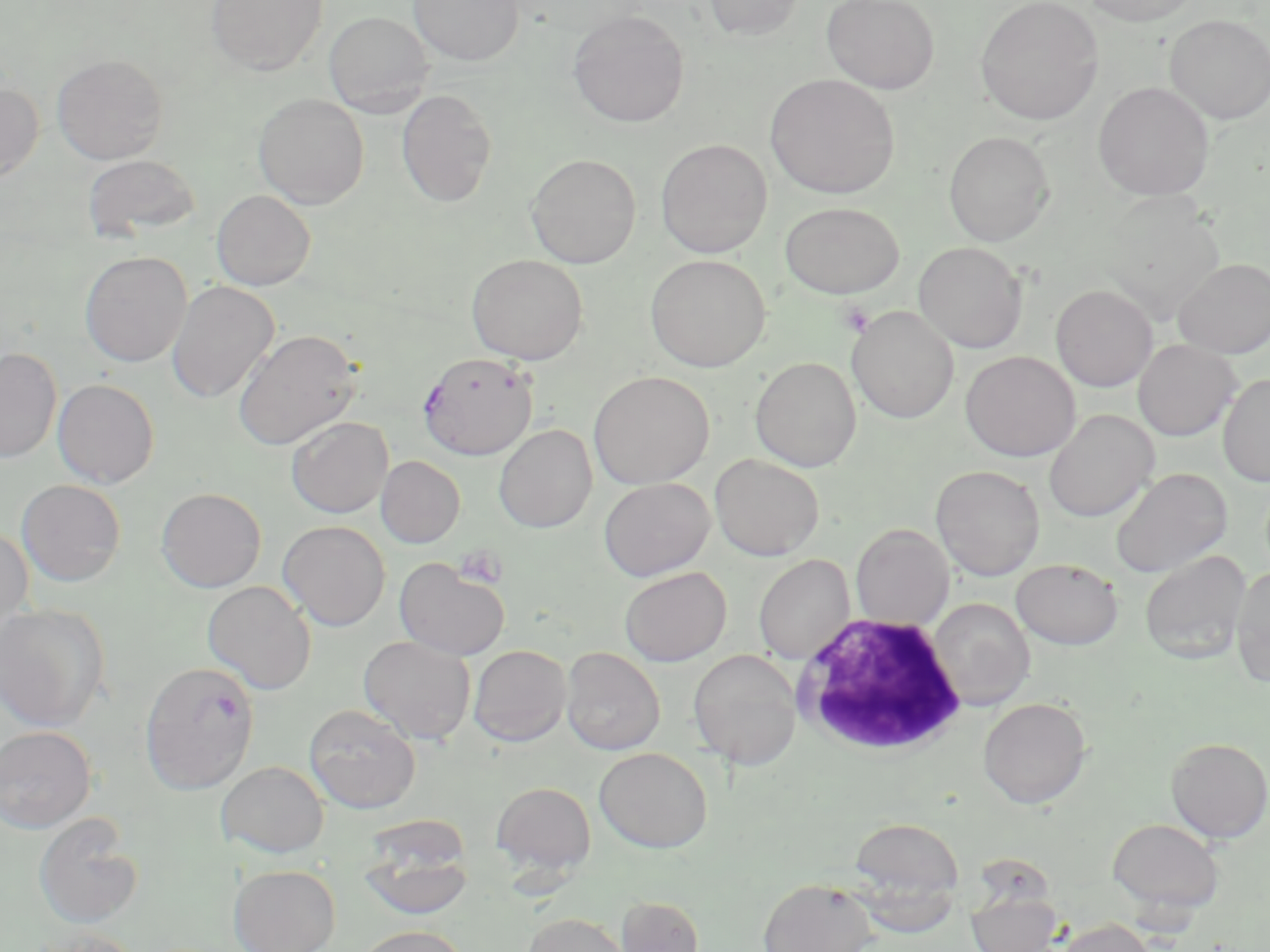
slide_level_diagnosis: Plasmodium falciparum
white_blood_cell_locations: 'approximate bounding boxes as named x1/y1/x2/y2 corners in pixels: (x1=791, y1=613, x2=969, y2=759)'
platelet_locations: 'approximate bounding boxes as named x1/y1/x2/y2 corners in pixels: (x1=838, y1=300, x2=874, y2=337), (x1=454, y1=546, x2=508, y2=588)'
magnification: 1000x
uninfected_red_blood_cell_locations: 'approximate bounding boxes as named x1/y1/x2/y2 corners in pixels: (x1=206, y1=0, x2=328, y2=76), (x1=408, y1=0, x2=523, y2=65), (x1=704, y1=0, x2=806, y2=40), (x1=822, y1=0, x2=940, y2=94), (x1=975, y1=0, x2=1103, y2=125), (x1=1080, y1=0, x2=1203, y2=26), (x1=324, y1=10, x2=433, y2=116), (x1=568, y1=10, x2=690, y2=128), (x1=1165, y1=14, x2=1270, y2=123), (x1=51, y1=53, x2=168, y2=165), (x1=765, y1=73, x2=900, y2=198), (x1=0, y1=81, x2=43, y2=184), (x1=1093, y1=81, x2=1214, y2=201), (x1=396, y1=88, x2=497, y2=207), (x1=253, y1=93, x2=369, y2=209), (x1=943, y1=130, x2=1055, y2=246), (x1=655, y1=138, x2=773, y2=258), (x1=526, y1=153, x2=641, y2=268), (x1=82, y1=154, x2=202, y2=241), (x1=211, y1=190, x2=315, y2=290), (x1=779, y1=202, x2=904, y2=299), (x1=913, y1=241, x2=1027, y2=353), (x1=79, y1=251, x2=192, y2=367), (x1=467, y1=253, x2=588, y2=364), (x1=645, y1=254, x2=770, y2=372), (x1=1172, y1=258, x2=1270, y2=358), (x1=167, y1=280, x2=279, y2=403), (x1=1051, y1=284, x2=1158, y2=391), (x1=846, y1=306, x2=959, y2=423), (x1=233, y1=329, x2=361, y2=450), (x1=1133, y1=339, x2=1240, y2=441), (x1=0, y1=347, x2=62, y2=464), (x1=960, y1=351, x2=1080, y2=461), (x1=750, y1=357, x2=862, y2=472), (x1=589, y1=371, x2=714, y2=489), (x1=1218, y1=373, x2=1270, y2=486), (x1=53, y1=379, x2=160, y2=487), (x1=1043, y1=409, x2=1159, y2=522), (x1=285, y1=416, x2=393, y2=518), (x1=494, y1=424, x2=598, y2=533), (x1=710, y1=453, x2=825, y2=561), (x1=376, y1=455, x2=465, y2=548), (x1=930, y1=464, x2=1045, y2=580), (x1=1111, y1=468, x2=1232, y2=578), (x1=598, y1=477, x2=715, y2=581), (x1=16, y1=479, x2=126, y2=586), (x1=156, y1=487, x2=266, y2=592), (x1=278, y1=520, x2=390, y2=631), (x1=850, y1=523, x2=953, y2=629), (x1=0, y1=526, x2=34, y2=636), (x1=1139, y1=550, x2=1251, y2=663), (x1=754, y1=554, x2=855, y2=664), (x1=394, y1=557, x2=511, y2=661), (x1=1011, y1=558, x2=1124, y2=649), (x1=1230, y1=565, x2=1270, y2=688), (x1=619, y1=566, x2=731, y2=666), (x1=202, y1=580, x2=316, y2=694), (x1=928, y1=598, x2=1035, y2=709), (x1=0, y1=603, x2=111, y2=732), (x1=358, y1=635, x2=476, y2=744), (x1=468, y1=644, x2=571, y2=747), (x1=561, y1=647, x2=665, y2=755), (x1=688, y1=649, x2=802, y2=769), (x1=978, y1=697, x2=1091, y2=808), (x1=303, y1=703, x2=421, y2=813), (x1=0, y1=726, x2=97, y2=833), (x1=1165, y1=737, x2=1269, y2=843), (x1=594, y1=747, x2=713, y2=853), (x1=216, y1=760, x2=329, y2=858), (x1=491, y1=782, x2=596, y2=876), (x1=33, y1=813, x2=144, y2=929), (x1=848, y1=817, x2=965, y2=911), (x1=1108, y1=818, x2=1223, y2=916), (x1=360, y1=832, x2=473, y2=920), (x1=228, y1=864, x2=340, y2=952), (x1=758, y1=877, x2=877, y2=952), (x1=966, y1=891, x2=1062, y2=952), (x1=615, y1=896, x2=704, y2=951), (x1=523, y1=913, x2=632, y2=952), (x1=1056, y1=918, x2=1158, y2=952), (x1=356, y1=925, x2=468, y2=952), (x1=29, y1=927, x2=143, y2=952)'
preparation: thin blood smear
modality: light microscopy
stain: May-Grünwald-Giemsa
image_size: 1270×952 pixels
plasmodium_falciparum_infected_red_blood_cell_locations: 'approximate bounding boxes as named x1/y1/x2/y2 corners in pixels: (x1=418, y1=351, x2=538, y2=460), (x1=139, y1=660, x2=259, y2=794)'
field_of_view: single